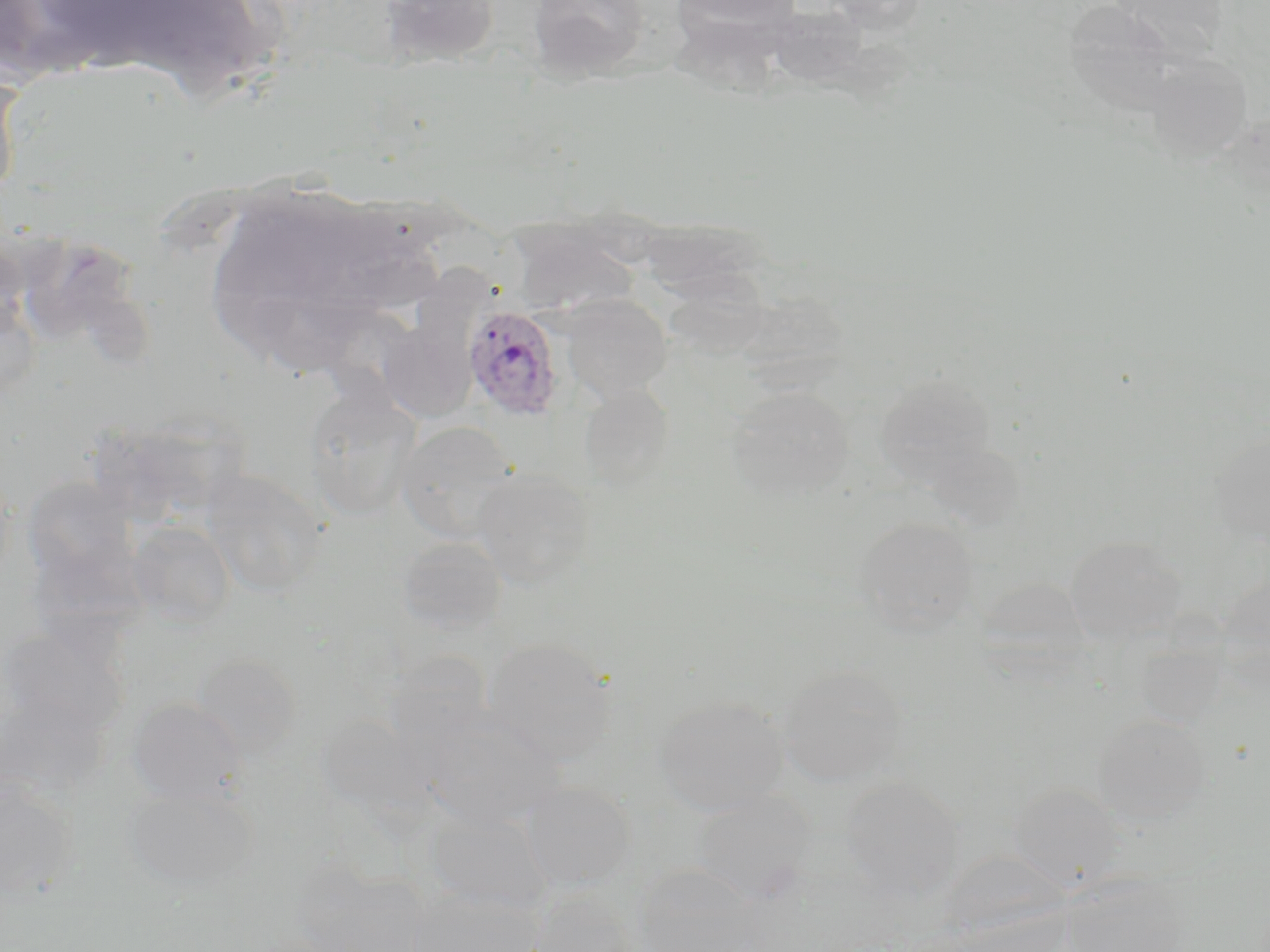

Summary:
  - Coordinate format: approximate bounding boxes as (x1,y1)-(x2,y2) corner pairs in pixels
  - Plasmodium ovale-infected red blood cell locations: (463,305)-(565,420)
  - Uninfected red blood cell locations: (380,0)-(502,67), (527,0)-(651,81), (671,0)-(801,37), (816,0)-(928,33), (1105,0)-(1232,59), (766,5)-(869,89), (1145,53)-(1255,163), (0,66)-(26,204), (511,229)-(637,318), (563,296)-(671,401), (380,317)-(477,422), (875,373)-(994,483), (579,384)-(674,490), (303,386)-(420,520), (727,386)-(855,501), (396,420)-(519,542), (1209,427)-(1270,550), (926,440)-(1027,531), (472,467)-(595,589), (201,469)-(327,597), (21,477)-(139,586), (855,516)-(979,636), (128,520)-(235,626), (395,535)-(507,636), (1064,535)-(1187,644), (24,541)-(152,657), (1215,569)-(1270,683), (974,575)-(1091,664), (0,627)-(130,740), (1132,633)-(1228,727), (484,637)-(617,764), (384,649)-(491,744), (192,653)-(302,759), (776,663)-(909,787), (0,691)-(107,801), (654,696)-(788,816), (127,697)-(246,806), (418,709)-(565,829), (315,713)-(436,825), (1092,714)-(1211,826), (0,776)-(78,901), (840,776)-(965,902), (521,781)-(636,890), (124,782)-(258,893), (1009,782)-(1122,890), (689,789)-(818,904), (424,806)-(551,913), (940,849)-(1067,944), (292,861)-(428,952), (632,863)-(760,951), (1057,871)-(1193,951), (408,887)-(541,952), (527,890)-(645,952)
  - Slide-level diagnosis: Plasmodium ovale
  - Magnification: 1000x
  - Modality: optical microscopy
  - Preparation: thin blood film
  - Field of view: single
  - Stain: May-Grünwald-Giemsa
  - Image size: 1270×952 pixels